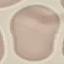

result = no malaria parasites detected
image type = cell patch, automatically extracted from a larger field of view and resized to 64 × 64 pixels
stain = Giemsa
capture = smartphone through the microscope eyepiece
preparation = thin blood film